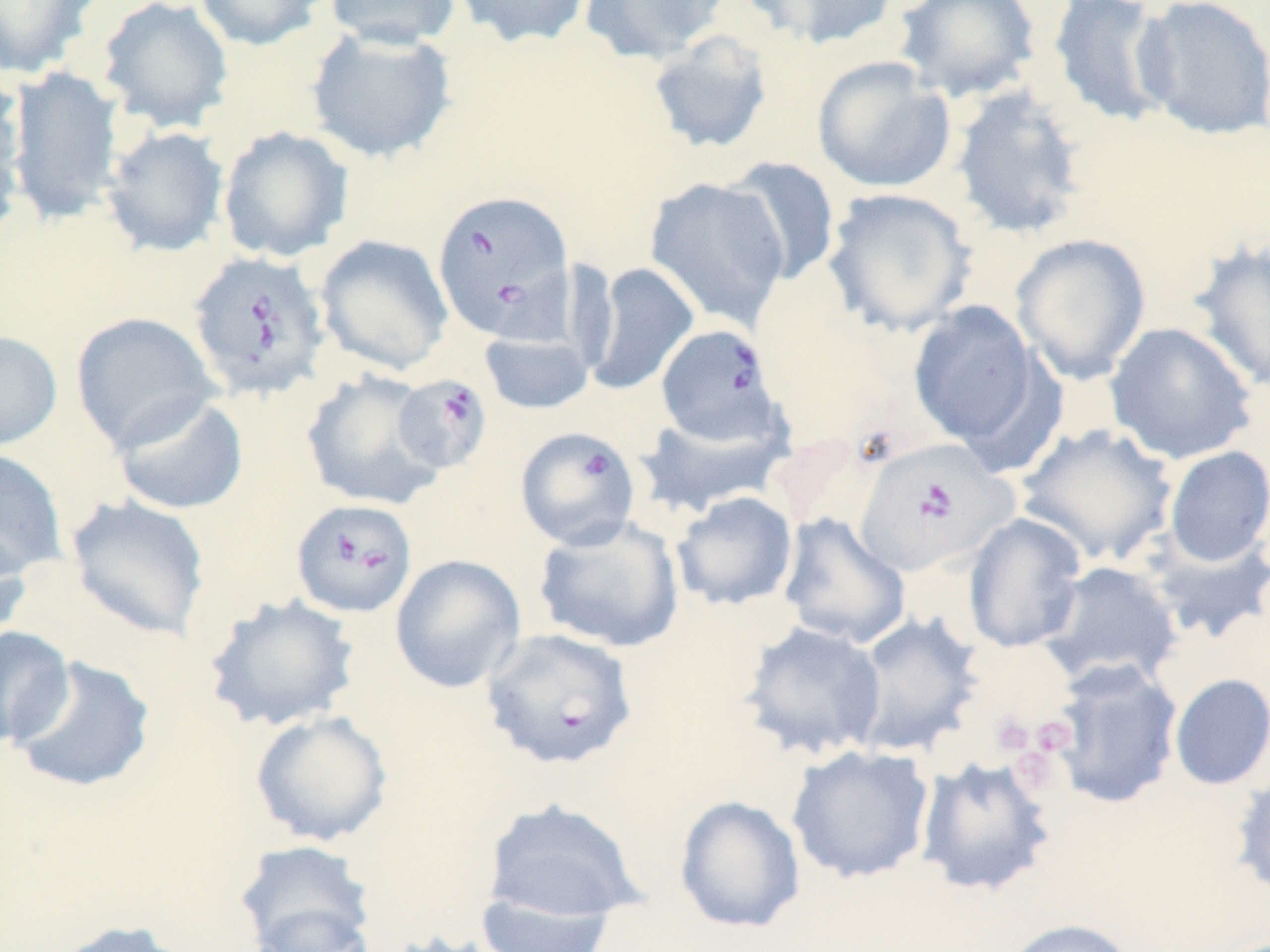
slide-level diagnosis = Babesia divergens
modality = light microscopy
platelet locations = approximate bounding boxes as (x1, y1, x2, y2) in pixels: (990, 712, 1035, 755), (1032, 716, 1078, 755), (1013, 752, 1054, 792)
stain = May-Grünwald-Giemsa
Babesia divergens-infected red blood cell locations = approximate bounding boxes as (x1, y1, x2, y2) in pixels: (431, 189, 575, 341), (187, 250, 332, 403), (655, 323, 784, 447), (392, 373, 493, 474), (514, 425, 643, 551), (852, 439, 1017, 577), (290, 498, 418, 617), (479, 627, 639, 770)
image size = 1270×952 pixels
magnification = 1000x
preparation = thin blood film
field of view = single
uninfected red blood cell locations = approximate bounding boxes as (x1, y1, x2, y2) in pixels: (0, 0, 100, 79), (97, 0, 234, 134), (194, 0, 329, 50), (323, 0, 462, 50), (451, 0, 594, 49), (579, 0, 729, 65), (742, 0, 899, 51), (892, 0, 1042, 102), (1046, 0, 1177, 128), (1133, 0, 1270, 141), (306, 28, 457, 164), (646, 31, 774, 155), (811, 55, 956, 194), (5, 65, 125, 225), (950, 85, 1090, 240), (0, 92, 25, 249), (217, 125, 354, 263), (100, 126, 230, 258), (722, 156, 842, 286), (645, 176, 791, 330), (821, 187, 978, 336), (1011, 233, 1151, 384), (315, 234, 454, 376), (1188, 237, 1270, 394), (585, 262, 699, 396), (907, 300, 1045, 453), (70, 312, 220, 453), (1104, 321, 1258, 465), (0, 330, 63, 451), (478, 330, 595, 415), (300, 369, 445, 511), (112, 393, 249, 515), (632, 407, 791, 518), (1016, 423, 1179, 567), (1163, 446, 1270, 568), (0, 448, 68, 580), (671, 491, 799, 611), (64, 494, 212, 643), (776, 512, 911, 650), (962, 513, 1088, 653), (532, 515, 685, 654), (0, 525, 33, 647), (1141, 526, 1270, 646), (389, 553, 526, 693), (1037, 560, 1184, 690), (202, 593, 361, 734), (847, 610, 986, 760), (737, 620, 888, 762), (0, 625, 75, 749), (9, 655, 156, 794), (1046, 659, 1184, 809), (1168, 673, 1270, 791), (249, 709, 393, 847), (786, 745, 935, 884), (914, 755, 1059, 898), (1231, 765, 1270, 900), (674, 795, 806, 934), (480, 798, 648, 925), (231, 839, 378, 951), (473, 891, 619, 951), (246, 903, 378, 952), (1001, 918, 1138, 952), (49, 919, 201, 952)